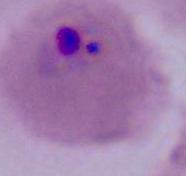

modality = photomicrograph
magnification = 400x or 1000x
identification = Plasmodium